Assess this cell for malaria.
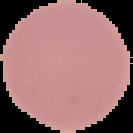
Uninfected.

Summary:
  - Preparation: thin blood smear
  - Image type: cell region segmented out of the field of view; surrounding area masked to black
  - Image size: 133×133 pixels